Locate platelets.
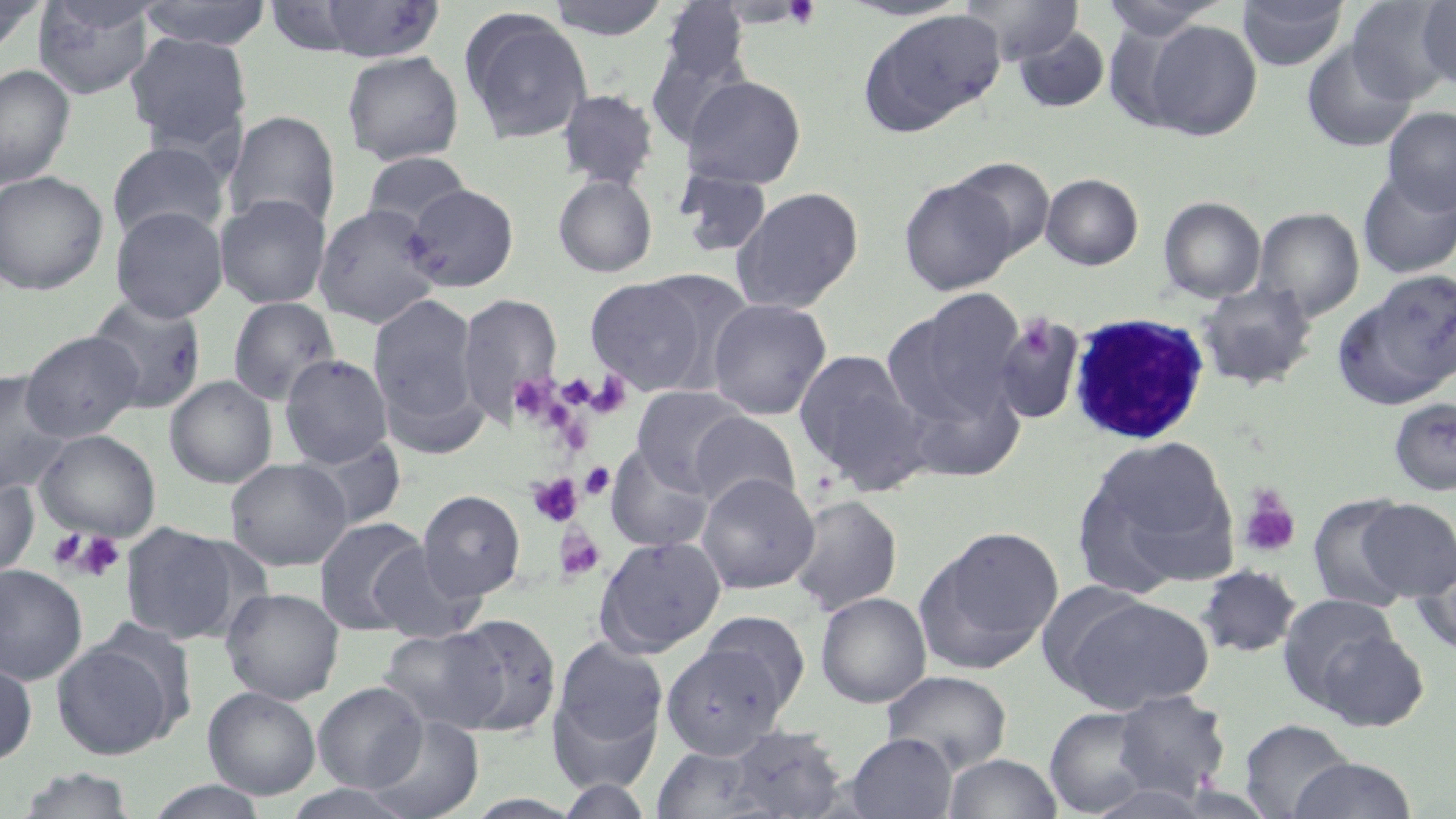

Approximate bounding boxes as (x1, y1, x2, y2) in pixels.
Platelets: (782, 0, 820, 29), (1016, 316, 1056, 360), (584, 371, 633, 419), (508, 374, 559, 422), (580, 462, 615, 499), (527, 473, 583, 527), (1237, 487, 1301, 558), (555, 525, 606, 582), (47, 529, 88, 570), (69, 530, 126, 581).

slide-level diagnosis = Plasmodium malariae
white blood cell locations = approximate bounding boxes as (x1, y1, x2, y2) in pixels: (1068, 311, 1211, 446)
uninfected red blood cell locations = approximate bounding boxes as (x1, y1, x2, y2) in pixels: (138, 0, 273, 50), (310, 0, 446, 62), (545, 0, 671, 41), (839, 0, 973, 22), (960, 0, 1082, 65), (1098, 0, 1229, 40), (1236, 0, 1349, 71), (1416, 0, 1456, 87), (0, 1, 46, 55), (32, 1, 157, 99), (657, 1, 750, 90), (1347, 2, 1453, 102), (459, 9, 593, 146), (860, 9, 1006, 134), (1141, 19, 1263, 141), (1012, 26, 1111, 113), (126, 32, 253, 153), (1302, 40, 1417, 152), (341, 50, 464, 165), (0, 63, 76, 188), (680, 74, 807, 189), (557, 88, 660, 191), (1382, 108, 1456, 215), (224, 110, 340, 233), (107, 141, 231, 243), (361, 151, 473, 232), (951, 158, 1055, 258), (1357, 168, 1456, 279), (675, 169, 773, 259), (0, 170, 109, 295), (1040, 173, 1144, 270), (552, 174, 658, 278), (899, 177, 1016, 295), (402, 183, 519, 292), (718, 184, 844, 418), (731, 187, 865, 313), (215, 193, 331, 308), (1158, 196, 1266, 303), (313, 203, 444, 328), (110, 206, 228, 322), (1254, 207, 1365, 320), (1338, 270, 1455, 407), (584, 275, 716, 395), (1197, 280, 1318, 391), (884, 291, 1025, 430), (368, 292, 483, 440), (457, 292, 563, 425), (85, 295, 208, 414), (227, 296, 340, 406), (706, 297, 832, 419), (992, 314, 1086, 426), (20, 330, 143, 442), (793, 349, 923, 484), (280, 354, 393, 468), (0, 370, 72, 496), (164, 375, 277, 488), (901, 379, 1026, 482), (631, 385, 751, 491), (1388, 397, 1456, 496), (687, 411, 801, 513), (35, 429, 161, 541), (1078, 435, 1239, 591), (295, 437, 407, 531), (606, 442, 715, 552), (225, 458, 352, 571), (697, 472, 819, 594), (0, 474, 40, 577), (418, 490, 526, 601), (1306, 493, 1419, 613), (787, 494, 902, 616), (1355, 497, 1456, 601), (314, 517, 430, 635), (118, 521, 247, 645), (914, 526, 1064, 675), (594, 535, 727, 657), (1411, 539, 1456, 658), (368, 543, 484, 644), (0, 564, 88, 685), (1195, 564, 1302, 658), (1034, 579, 1154, 690), (221, 587, 345, 704), (815, 592, 931, 708), (1276, 593, 1408, 716), (1055, 594, 1216, 714), (699, 610, 811, 712), (444, 614, 562, 737), (378, 626, 509, 734), (550, 636, 669, 774), (51, 638, 177, 759), (660, 643, 789, 759), (0, 658, 38, 766), (882, 669, 1012, 774), (313, 681, 427, 793), (203, 686, 321, 800), (1110, 690, 1232, 799), (1044, 705, 1160, 816), (364, 714, 484, 818), (1239, 718, 1355, 818), (718, 725, 850, 818), (845, 733, 957, 819), (942, 752, 1063, 818), (1287, 756, 1420, 818), (11, 767, 141, 818), (556, 777, 655, 818), (142, 780, 272, 819), (280, 784, 421, 819)
image size = 1456×819 pixels
field of view = one of a larger specimen
magnification = 1000x
stain = May-Grünwald-Giemsa
preparation = thin blood film
modality = light microscopy